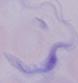

Summary:
  - Modality: micrograph
  - Identification: trypanosome
  - Magnification: 1000x